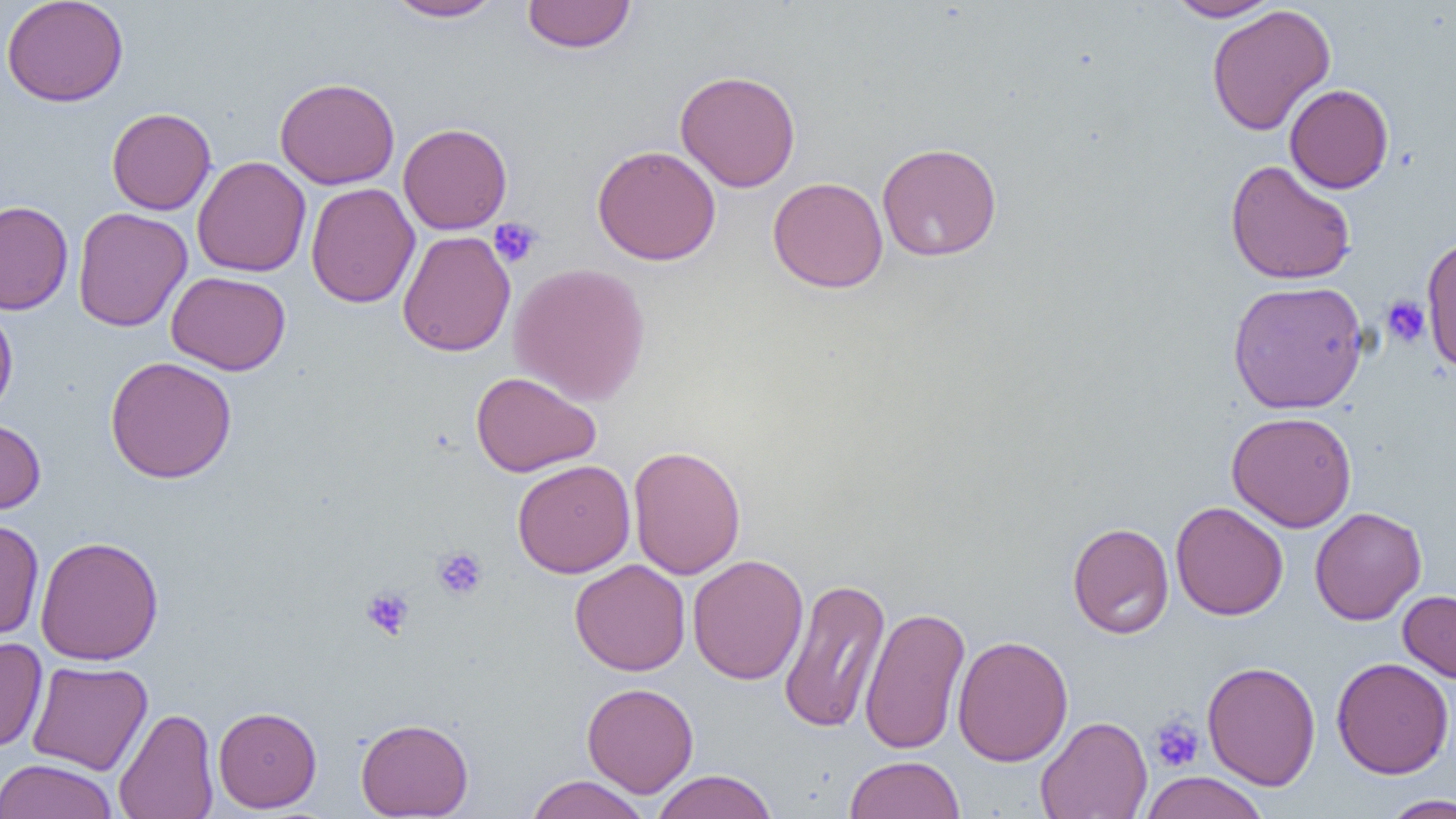

Summary:
  - Coordinate format: approximate bounding boxes as named x1/y1/x2/y2 corners in pixels
  - Platelet locations: (x1=489, y1=218, x2=542, y2=268), (x1=1381, y1=295, x2=1431, y2=347), (x1=432, y1=546, x2=488, y2=601), (x1=361, y1=587, x2=414, y2=639), (x1=1149, y1=715, x2=1205, y2=773)
  - Uninfected red blood cell locations: (x1=1, y1=0, x2=129, y2=107), (x1=384, y1=0, x2=505, y2=22), (x1=1165, y1=0, x2=1282, y2=22), (x1=521, y1=1, x2=636, y2=53), (x1=1206, y1=4, x2=1336, y2=136), (x1=675, y1=70, x2=801, y2=192), (x1=275, y1=77, x2=400, y2=189), (x1=1284, y1=84, x2=1394, y2=194), (x1=106, y1=107, x2=217, y2=215), (x1=398, y1=122, x2=512, y2=235), (x1=877, y1=142, x2=1002, y2=261), (x1=592, y1=144, x2=721, y2=266), (x1=192, y1=156, x2=311, y2=277), (x1=1225, y1=159, x2=1356, y2=285), (x1=767, y1=176, x2=888, y2=293), (x1=306, y1=182, x2=420, y2=308), (x1=0, y1=201, x2=74, y2=315), (x1=73, y1=207, x2=192, y2=332), (x1=397, y1=230, x2=516, y2=357), (x1=1421, y1=235, x2=1456, y2=372), (x1=508, y1=262, x2=651, y2=406), (x1=166, y1=271, x2=291, y2=375), (x1=1227, y1=280, x2=1368, y2=414), (x1=0, y1=302, x2=18, y2=420), (x1=105, y1=355, x2=237, y2=484), (x1=470, y1=371, x2=601, y2=476), (x1=1226, y1=411, x2=1357, y2=532), (x1=0, y1=418, x2=46, y2=514), (x1=628, y1=444, x2=746, y2=580), (x1=512, y1=459, x2=635, y2=578), (x1=1170, y1=501, x2=1288, y2=620), (x1=1309, y1=506, x2=1426, y2=625), (x1=0, y1=518, x2=45, y2=641), (x1=1067, y1=522, x2=1174, y2=639), (x1=35, y1=536, x2=164, y2=665), (x1=688, y1=554, x2=809, y2=685), (x1=570, y1=559, x2=691, y2=676), (x1=778, y1=577, x2=891, y2=734), (x1=1398, y1=589, x2=1456, y2=683), (x1=860, y1=606, x2=970, y2=756), (x1=952, y1=635, x2=1073, y2=766), (x1=0, y1=637, x2=47, y2=752), (x1=1331, y1=657, x2=1453, y2=779), (x1=27, y1=660, x2=153, y2=775), (x1=1202, y1=660, x2=1320, y2=791), (x1=582, y1=682, x2=698, y2=797), (x1=213, y1=706, x2=321, y2=813), (x1=114, y1=707, x2=219, y2=819), (x1=1036, y1=715, x2=1152, y2=819), (x1=355, y1=717, x2=474, y2=818), (x1=845, y1=755, x2=965, y2=819), (x1=0, y1=758, x2=119, y2=819), (x1=651, y1=769, x2=778, y2=819), (x1=1138, y1=771, x2=1269, y2=819), (x1=525, y1=774, x2=650, y2=819), (x1=1380, y1=794, x2=1456, y2=818)
  - Slide-level diagnosis: no evidence of blood parasites
  - Preparation: thin blood film
  - Magnification: 1000x
  - Image size: 1456×819 pixels
  - Field of view: single
  - Modality: optical microscopy